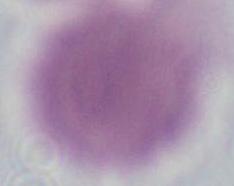

{
  "identification": "erythrocyte",
  "modality": "photomicrograph",
  "magnification": "1000x"
}